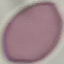

Malaria status: uninfected. Thin blood smear. Cell patch, automatically extracted from a larger field of view and resized to 64 × 64 pixels. Photographed with a smartphone camera at the microscope eyepiece. Giemsa stain.